Locate every leukocyte (white blood cell).
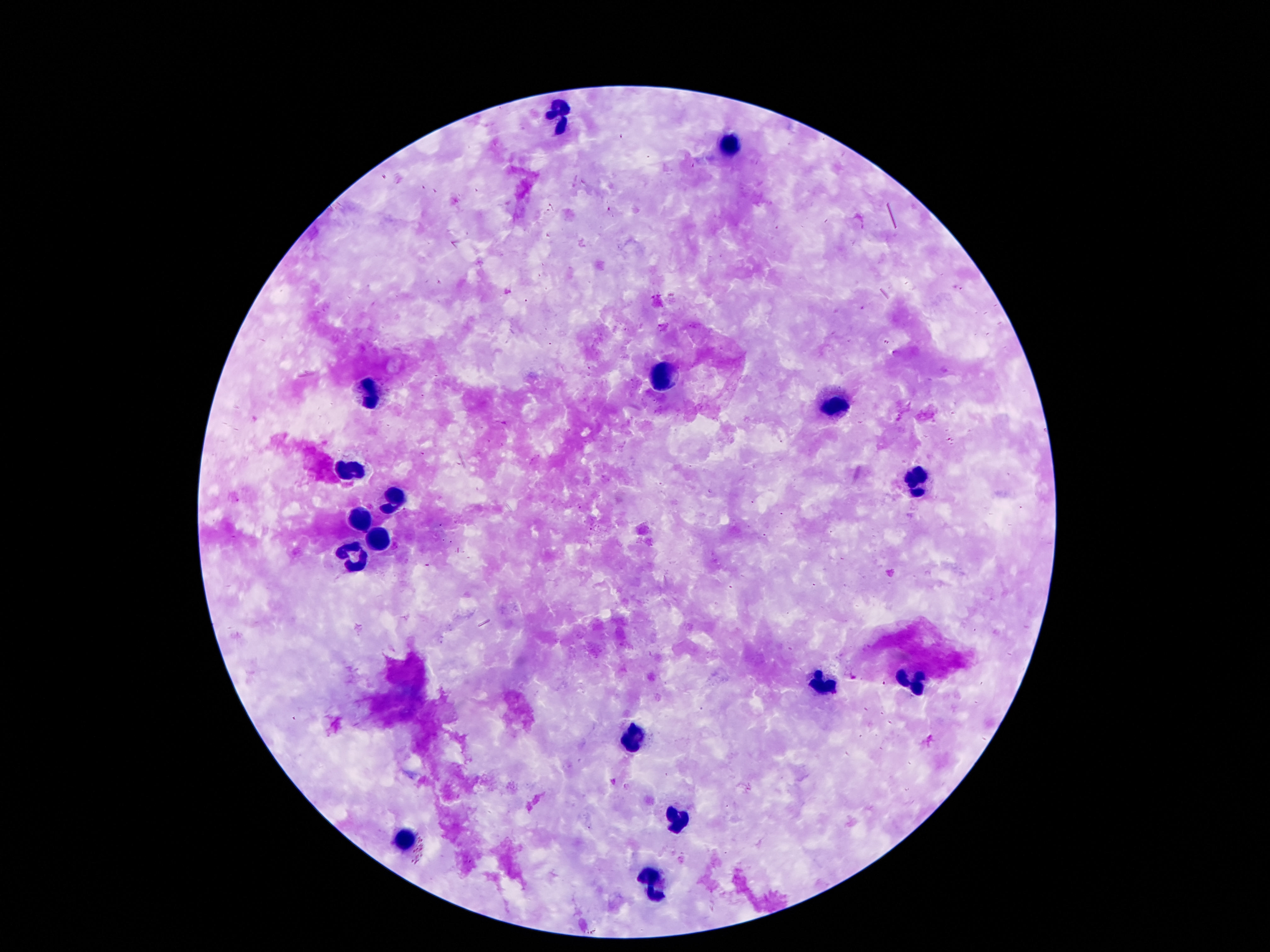

Approximate centers as [x, y] in pixels.
Leukocytes: [560, 114], [732, 143], [664, 378], [373, 393], [840, 407], [351, 469], [918, 479], [394, 497], [361, 522], [376, 539], [355, 559], [914, 682], [824, 684], [632, 737], [675, 819], [408, 840], [650, 883].

patient malaria status = uninfected
field of view = one from this slide
magnification = 100x
preparation = thick peripheral-blood smear
capture = smartphone camera through the microscope eyepiece
image size = 1270×952 pixels
stain = Giemsa